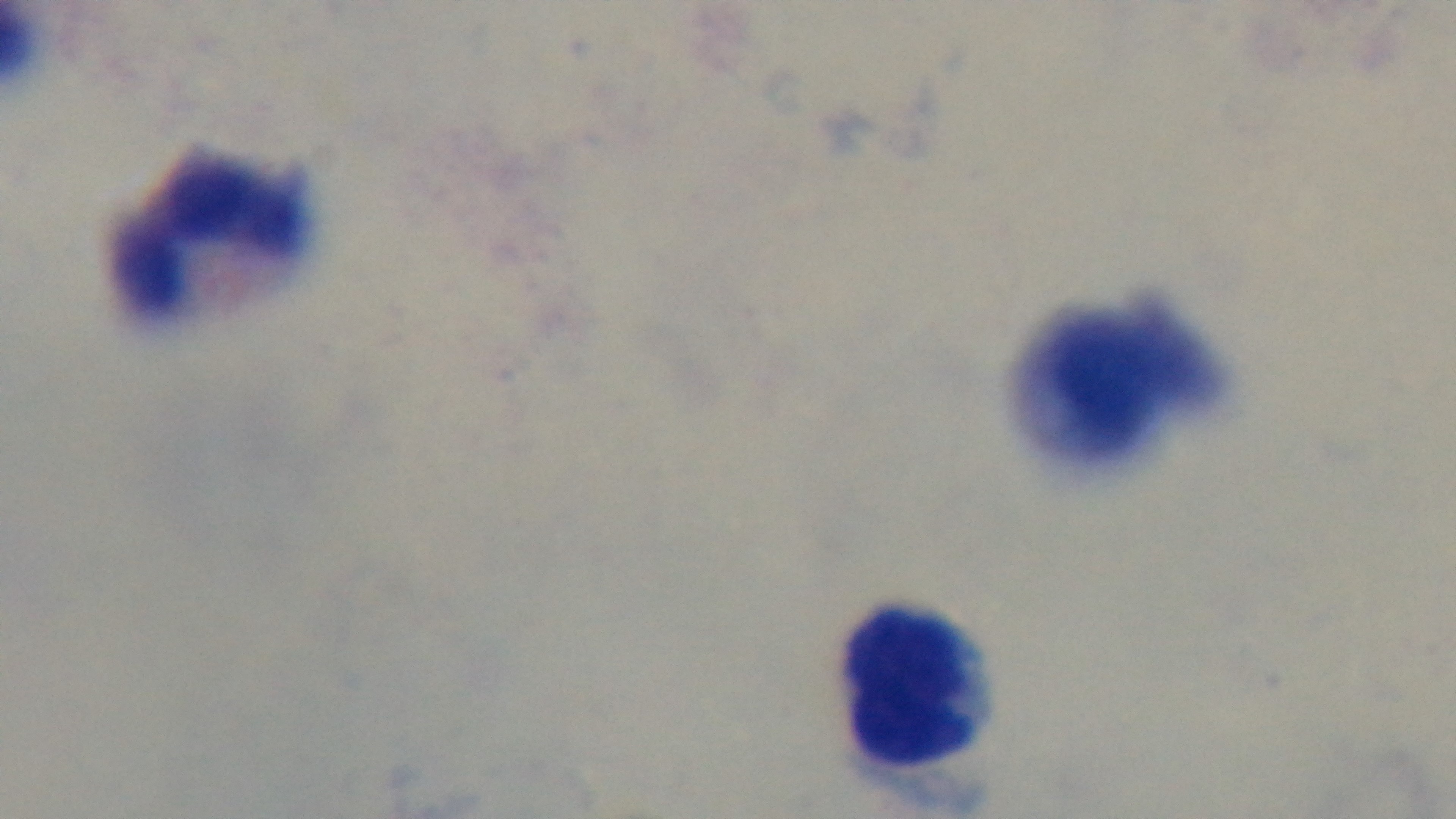 100x oil-immersion objective. Giemsa-stained. Photomicrograph. Preparation: thick blood film. Captured with a mounted 4K digital camera. One field from the slide. Malaria status: uninfected.